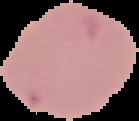

preparation = thin blood film
image size = 139×121 pixels
result = no Plasmodium parasites detected
image type = segmented cell region with the area outside set to black